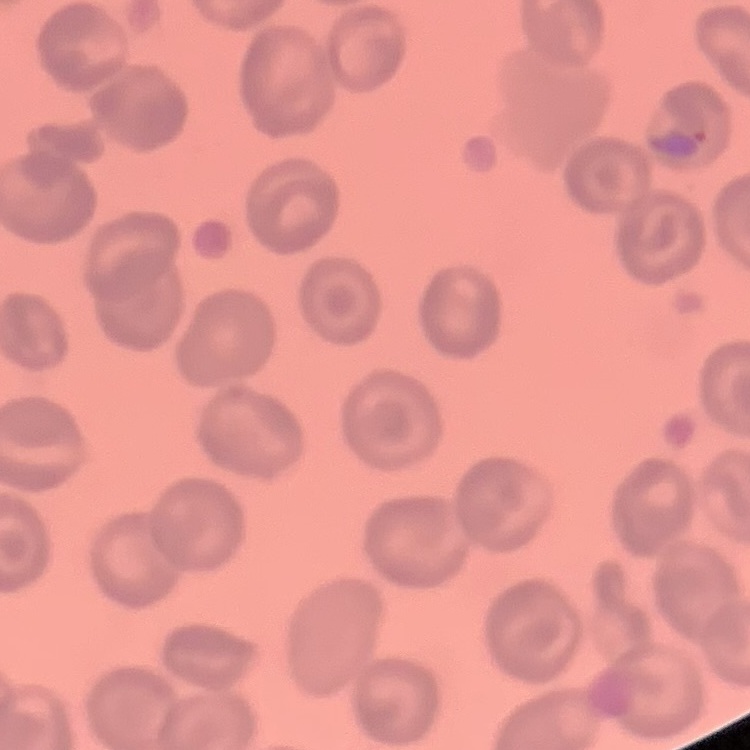
erythrocyte_morphology: no rouleaux formation
stain: Field's or Giemsa
image_type: one tile cut from a larger photomicrograph
preparation: thin blood smear